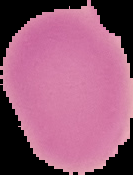 Malaria status: uninfected. Cell region segmented out of the field of view; the surrounding area is masked to black. From a thin blood film. Image is 133×175 pixels.